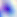 Toxoplasma gondii is shown. Photomicrograph. Captured at 400x magnification.